Comment on the morphology of the erythrocytes.
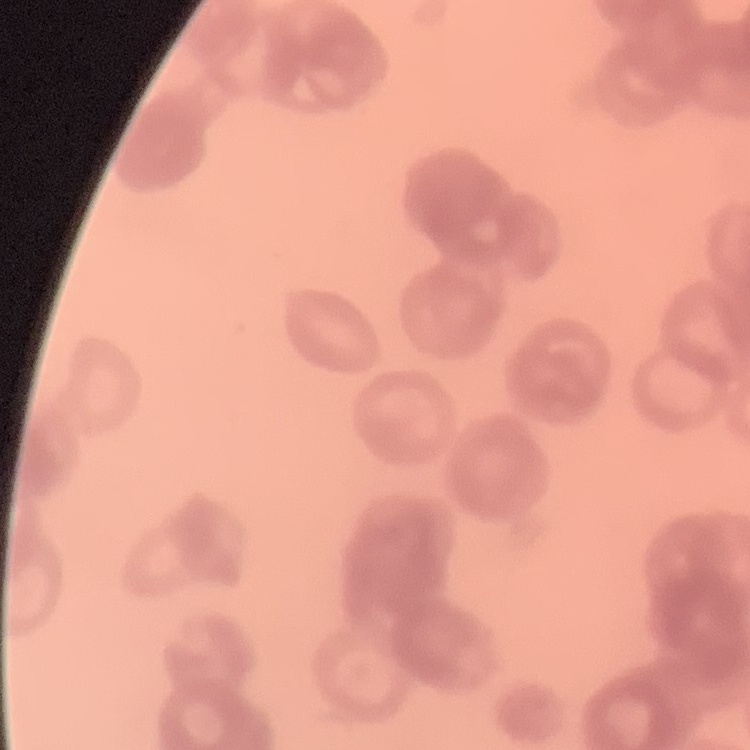
They show rouleaux formation.

Stained with either Field's or Giemsa. Square crop of a larger photomicrograph. Thin blood smear.